Assess the morphology of the red blood cells.
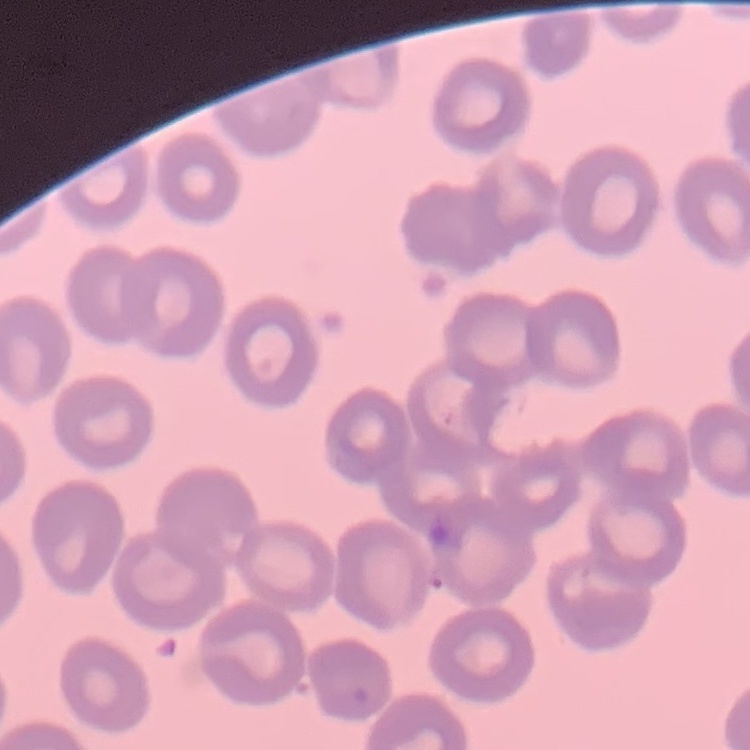

No rouleaux formation.

preparation = thin blood smear
image type = square crop of a larger photomicrograph
stain = Field's or Giemsa